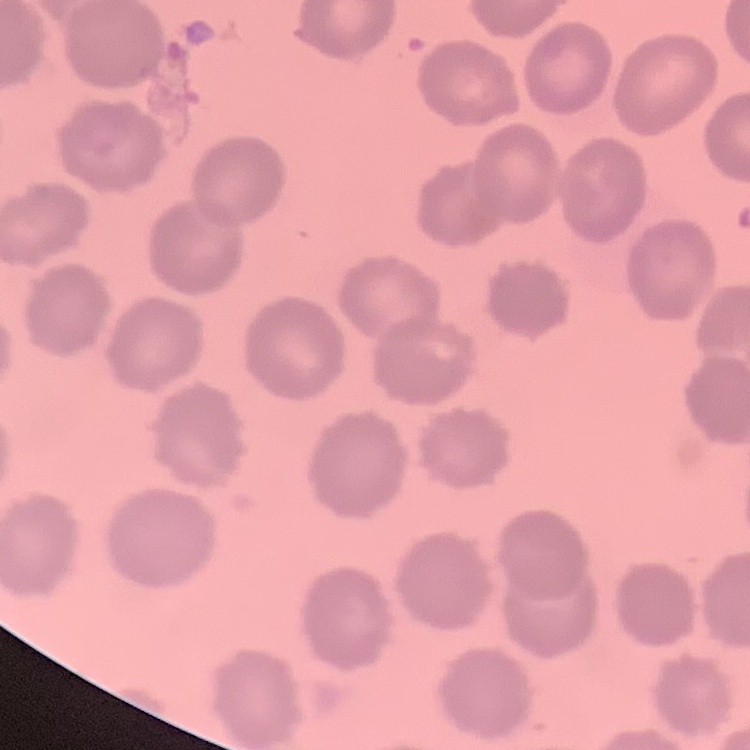

The erythrocytes show no rouleaux formation. Thin peripheral smear. Square crop of a larger photomicrograph. Field's or Giemsa stain.